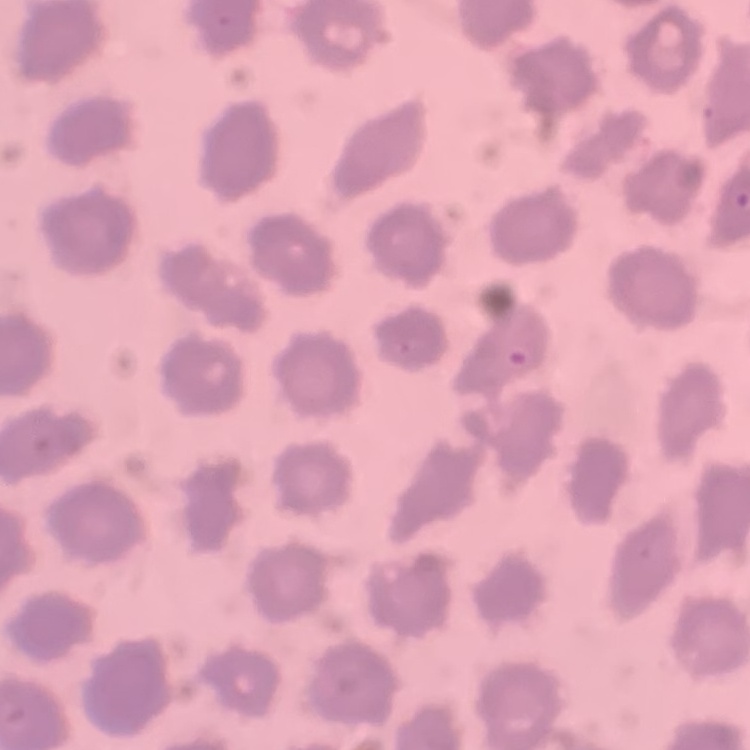
Summary:
  - Erythrocyte morphology: no rouleaux formation
  - Preparation: thin blood film
  - Image type: square crop of a larger photomicrograph
  - Stain: Field's or Giemsa